Assess this cell for malaria.
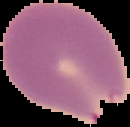

It is parasitized.

Summary:
  - Preparation: thin blood smear
  - Image size: 130×127 pixels
  - Image type: cell region segmented out of the field of view; surrounding area masked to black